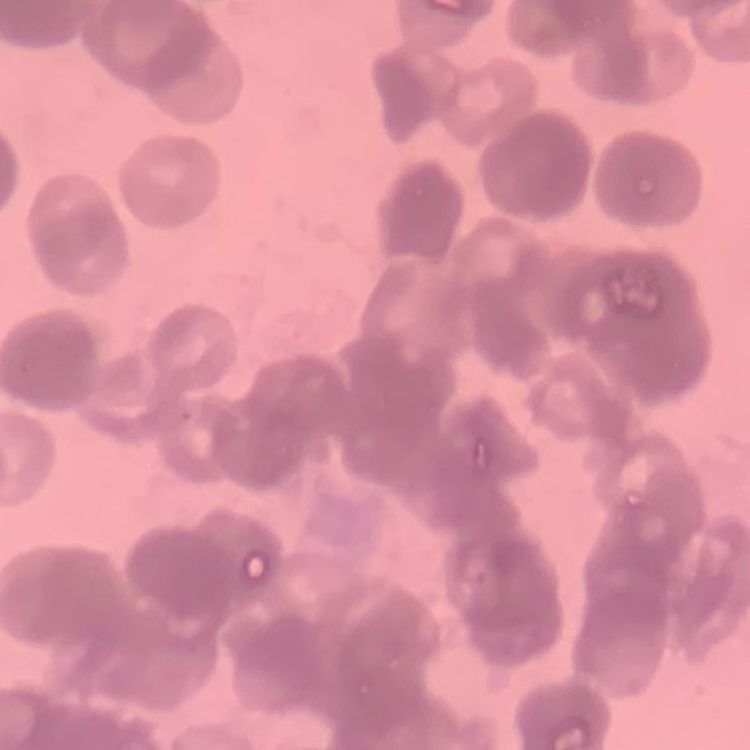 The red blood cells show rouleaux formation. Field's or Giemsa stain. Thin blood film. One tile cut from a larger photomicrograph.